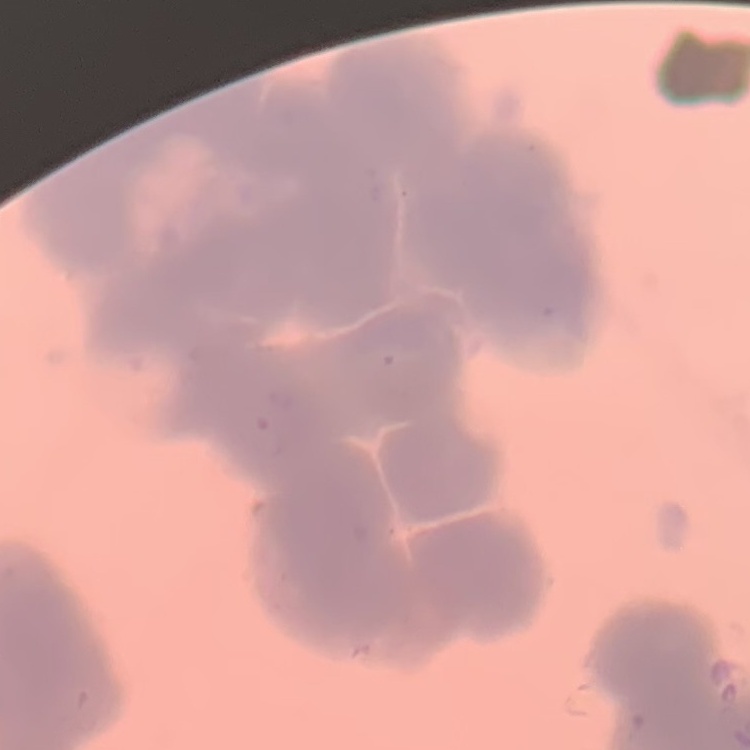

red blood cell morphology = rouleaux formation
image type = square crop of a larger photomicrograph
preparation = thin peripheral smear
stain = Field's or Giemsa